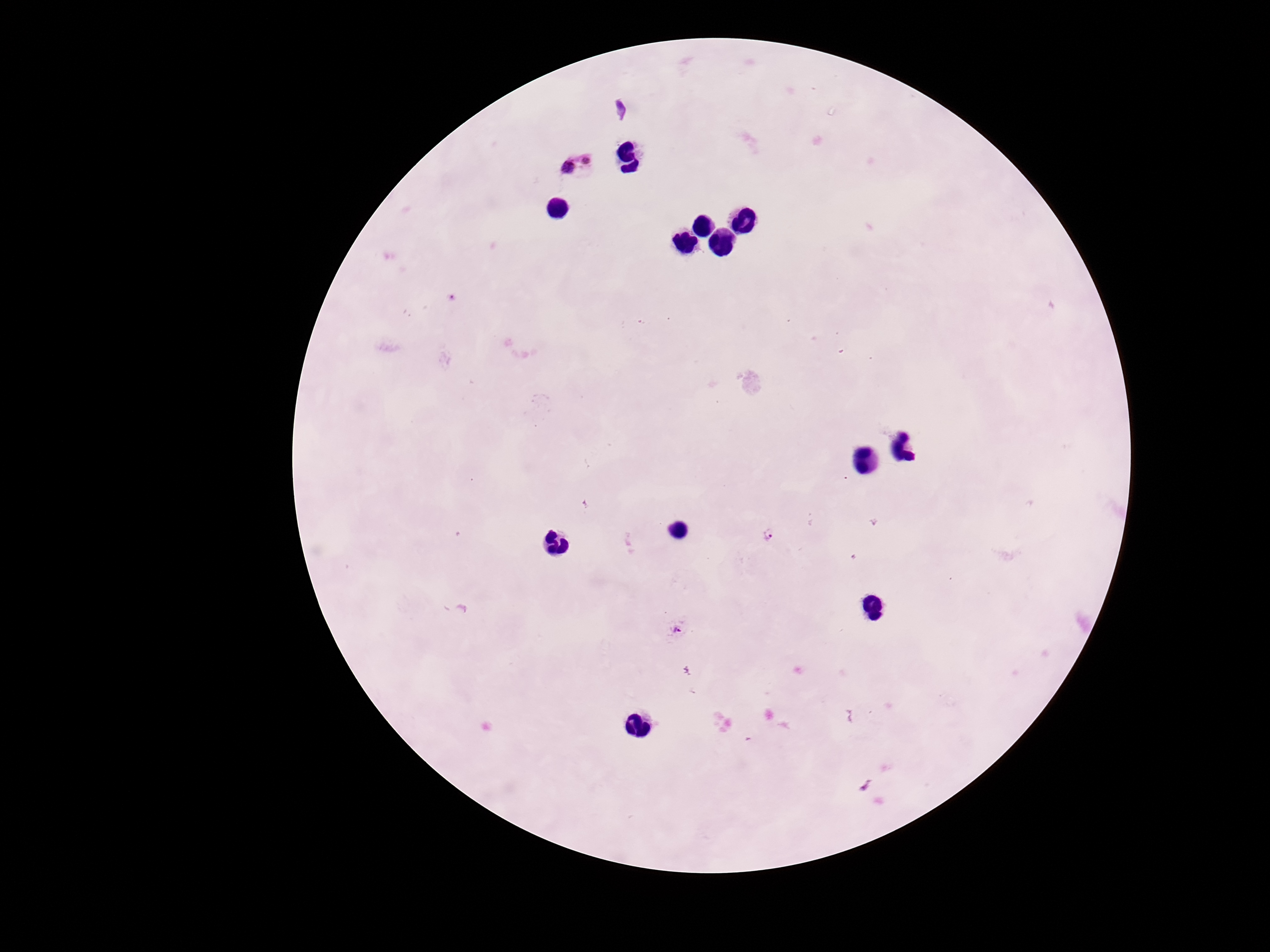 Approximate object centers, in pixels from the top-left corner. Plasmodium parasite locations: (x=575, y=164), (x=768, y=535), (x=678, y=629), (x=867, y=786). 100x magnification. Patient malaria status: positive. Smartphone photograph taken through the microscope eyepiece. Thick blood smear. Image is 1270×952 pixels. Giemsa-stained preparation. One field from this slide.